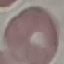

result = negative for malaria parasites
capture = smartphone through the microscope eyepiece
stain = Giemsa
image type = automatically extracted cell patch, resized to 64 × 64 pixels
preparation = thin smear